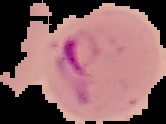

image type = segmented cell region with the area outside set to black
image size = 166×124 pixels
malaria status = parasitized
preparation = thin blood film